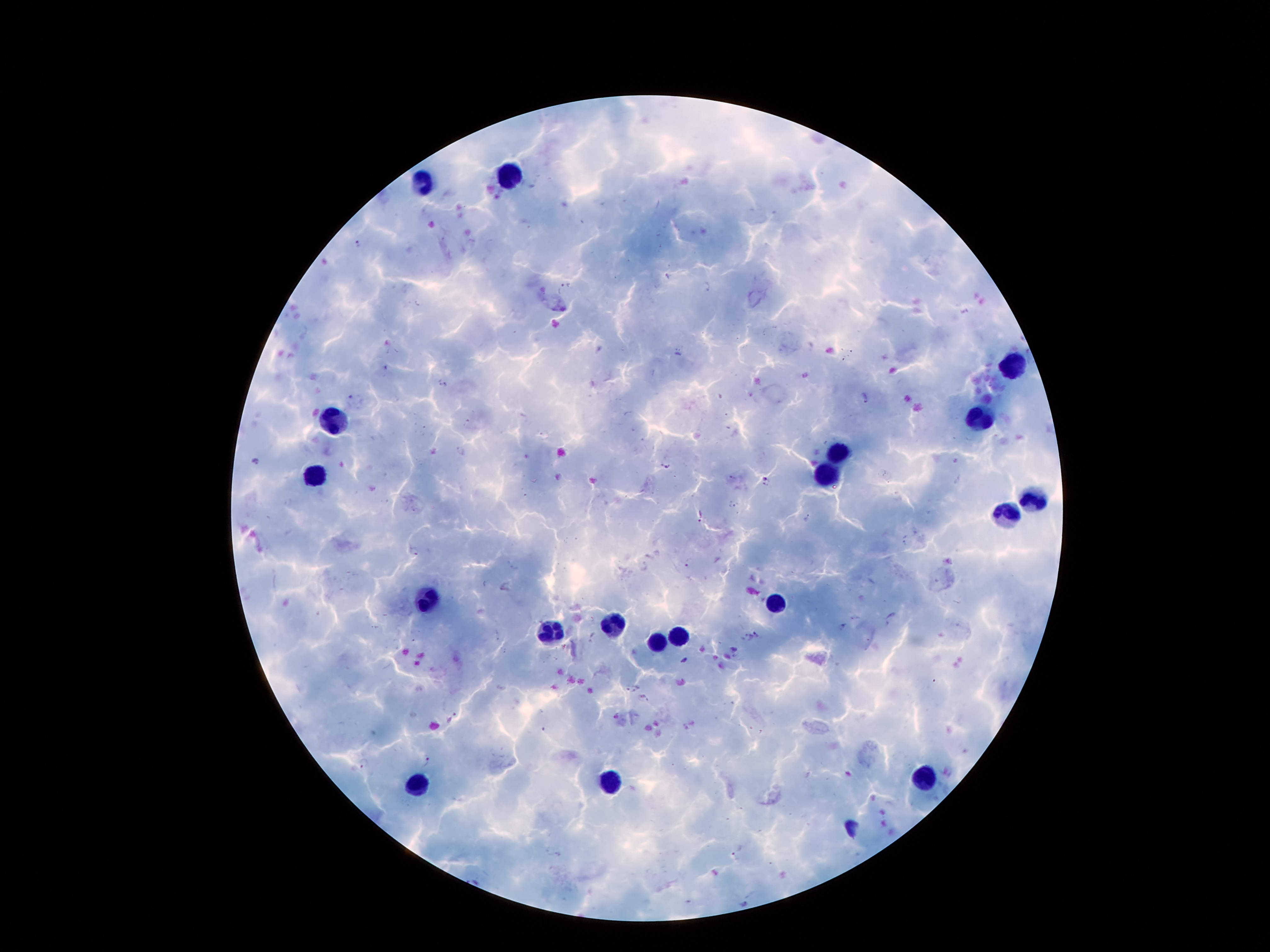

Approximate centers as (x, y) in pixels.
Summary:
  - Malaria parasite locations: (358, 244), (667, 276), (562, 287), (706, 287), (386, 368), (442, 383), (865, 398), (352, 400), (459, 452), (255, 461), (666, 466), (765, 481), (732, 506), (699, 517), (807, 518), (906, 542), (413, 552), (688, 563), (854, 617), (891, 617), (842, 627), (760, 634), (592, 637), (743, 638), (684, 660), (633, 687), (644, 700), (451, 718), (425, 762), (365, 763), (736, 850)
  - Leukocyte locations: (508, 176), (424, 181), (1012, 365), (328, 421), (980, 421), (837, 451), (315, 471), (824, 478), (1032, 501), (1005, 512), (431, 598), (776, 603), (612, 623), (553, 633), (681, 635), (656, 644), (926, 775), (419, 782), (610, 782)
  - Field of view: one from this slide
  - Stain: Giemsa
  - Image size: 1270×952 pixels
  - Capture: smartphone through the microscope eyepiece
  - Magnification: 100x
  - Patient malaria status: positive for Plasmodium falciparum
  - Preparation: thick blood film